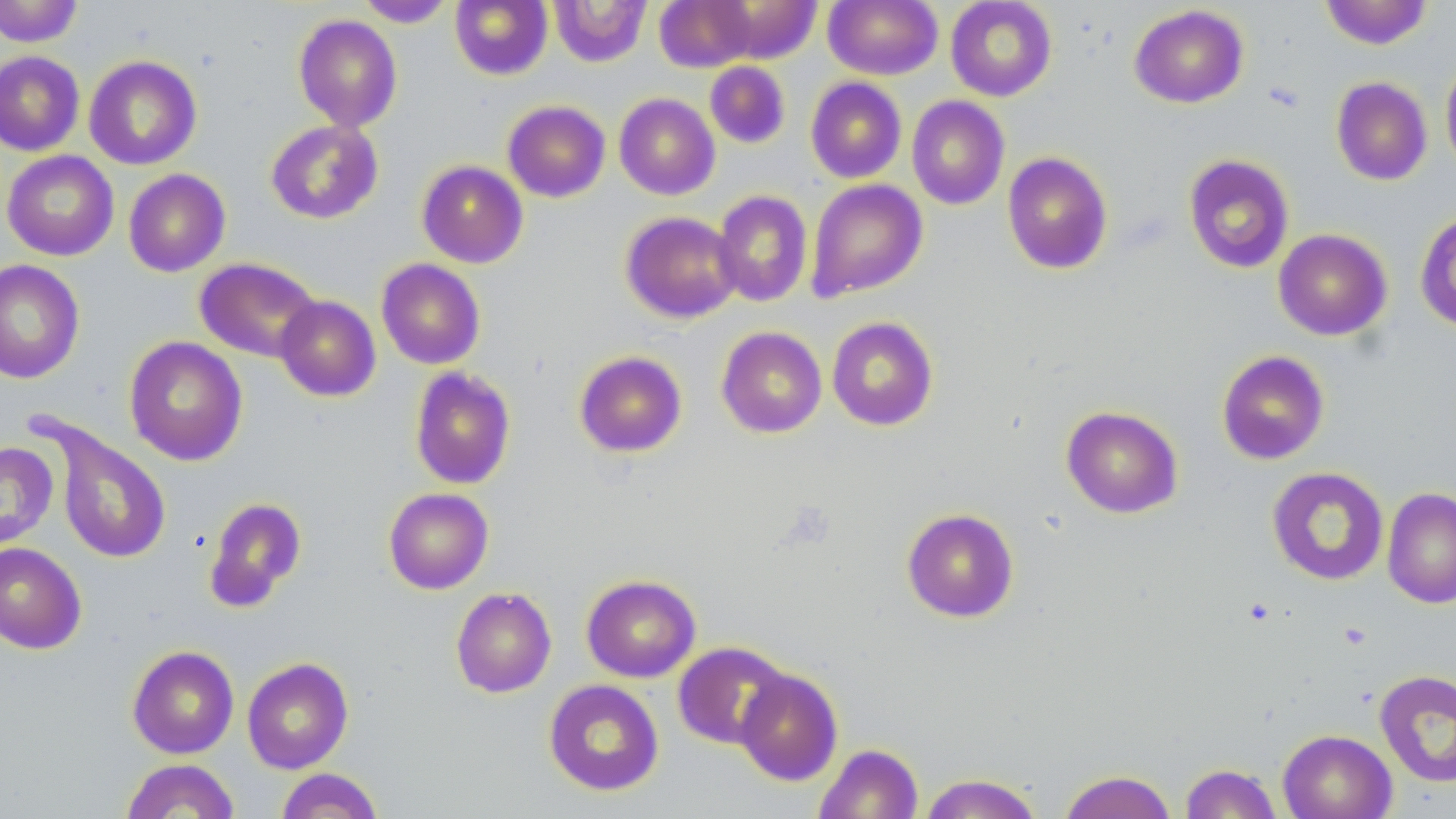

Approximate bounding boxes as named x1/y1/x2/y2 corners in pixels. Uninfected red blood cell locations: (x1=0, y1=0, x2=83, y2=47), (x1=450, y1=0, x2=553, y2=80), (x1=550, y1=0, x2=651, y2=67), (x1=654, y1=0, x2=755, y2=72), (x1=824, y1=0, x2=942, y2=80), (x1=945, y1=0, x2=1057, y2=101), (x1=1320, y1=0, x2=1433, y2=49), (x1=355, y1=1, x2=456, y2=27), (x1=711, y1=2, x2=821, y2=63), (x1=1129, y1=4, x2=1249, y2=108), (x1=293, y1=14, x2=403, y2=131), (x1=0, y1=51, x2=85, y2=156), (x1=84, y1=55, x2=202, y2=170), (x1=1440, y1=57, x2=1456, y2=177), (x1=704, y1=61, x2=791, y2=148), (x1=1331, y1=76, x2=1432, y2=186), (x1=805, y1=77, x2=907, y2=183), (x1=614, y1=93, x2=720, y2=200), (x1=907, y1=96, x2=1010, y2=210), (x1=502, y1=100, x2=611, y2=202), (x1=265, y1=119, x2=383, y2=224), (x1=2, y1=150, x2=119, y2=261), (x1=1002, y1=151, x2=1113, y2=275), (x1=1183, y1=154, x2=1294, y2=273), (x1=416, y1=160, x2=528, y2=268), (x1=123, y1=169, x2=231, y2=277), (x1=806, y1=178, x2=928, y2=301), (x1=712, y1=190, x2=813, y2=307), (x1=1414, y1=209, x2=1456, y2=332), (x1=620, y1=211, x2=742, y2=323), (x1=1273, y1=228, x2=1392, y2=341), (x1=194, y1=257, x2=322, y2=363), (x1=376, y1=258, x2=486, y2=370), (x1=0, y1=259, x2=85, y2=384), (x1=274, y1=296, x2=381, y2=401), (x1=826, y1=316, x2=939, y2=431), (x1=716, y1=326, x2=827, y2=438), (x1=124, y1=336, x2=248, y2=466), (x1=573, y1=350, x2=688, y2=457), (x1=1216, y1=350, x2=1330, y2=465), (x1=409, y1=366, x2=517, y2=490), (x1=1061, y1=405, x2=1184, y2=518), (x1=47, y1=424, x2=171, y2=565), (x1=1, y1=441, x2=58, y2=547), (x1=1267, y1=467, x2=1389, y2=586), (x1=383, y1=487, x2=494, y2=594), (x1=1382, y1=487, x2=1456, y2=609), (x1=203, y1=496, x2=307, y2=611), (x1=901, y1=507, x2=1020, y2=622), (x1=0, y1=542, x2=86, y2=654), (x1=581, y1=574, x2=701, y2=682), (x1=450, y1=587, x2=557, y2=698), (x1=672, y1=641, x2=791, y2=749), (x1=127, y1=645, x2=239, y2=759), (x1=242, y1=657, x2=354, y2=774), (x1=734, y1=669, x2=843, y2=785), (x1=1374, y1=669, x2=1456, y2=788), (x1=543, y1=679, x2=664, y2=796), (x1=1277, y1=729, x2=1397, y2=819), (x1=814, y1=743, x2=923, y2=819), (x1=120, y1=759, x2=240, y2=819), (x1=1180, y1=763, x2=1283, y2=818), (x1=275, y1=768, x2=384, y2=819), (x1=1059, y1=770, x2=1177, y2=819), (x1=918, y1=773, x2=1044, y2=818). Slide-level diagnosis: no evidence of blood parasites. Thin blood smear. Image is 1456×819 pixels. May-Grünwald-Giemsa stain. Optical microscopy. One field of a larger specimen. 1000x magnification.